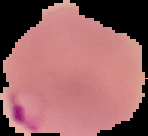
From a thin blood film. Result: Plasmodium parasites identified. Image is 148×136 pixels. Segmented cell region on a black background.